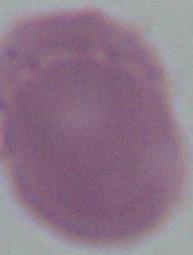
Summary:
  - Magnification: 1000x
  - Modality: photomicrograph
  - Identification: erythrocyte